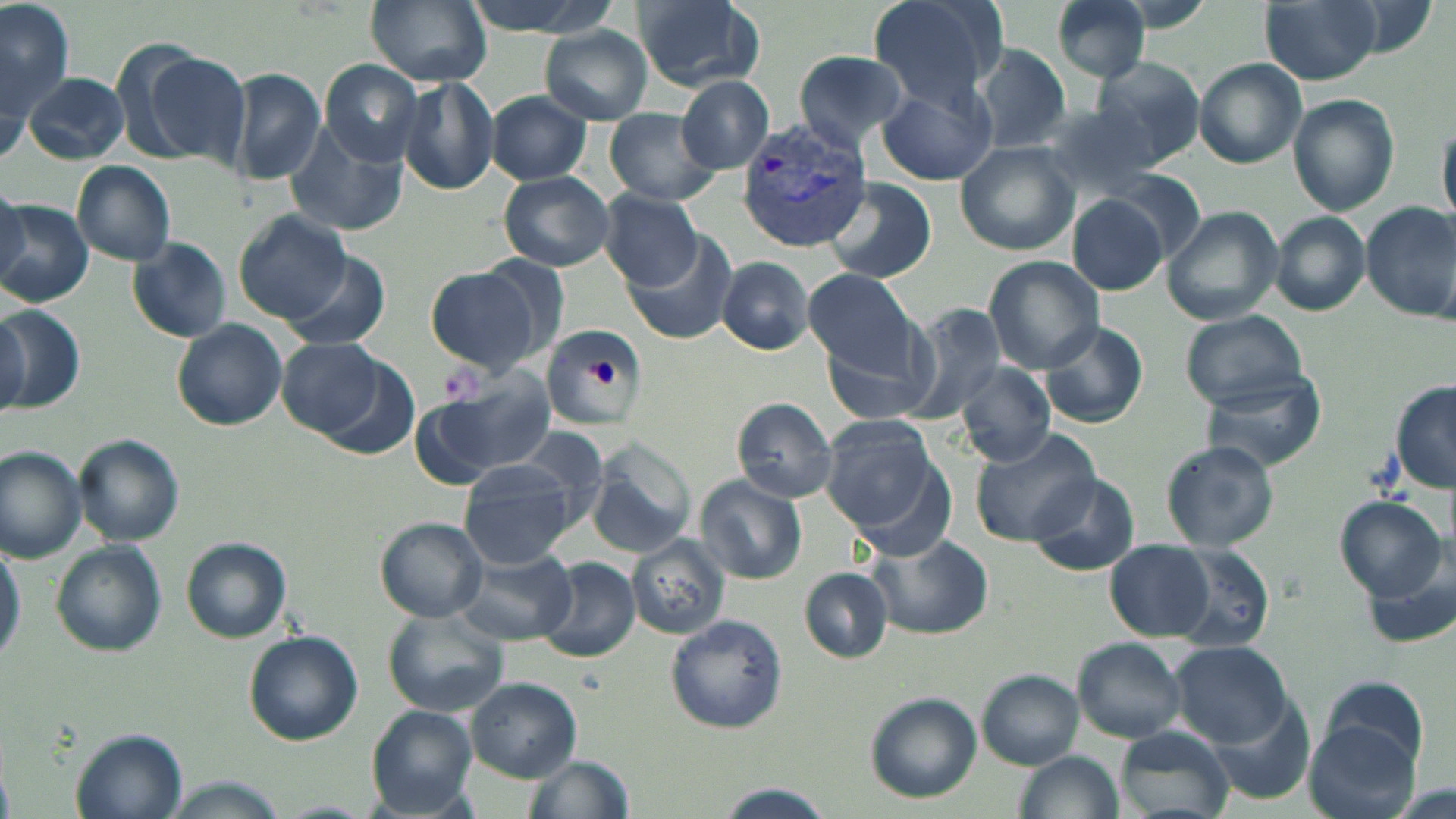
slide_level_diagnosis: Plasmodium vivax
field_of_view: single
magnification: 1000x
platelet_locations: 'approximate bounding boxes as (x1, y1, x2, y2) in pixels: (593, 356, 621, 388)'
uninfected_red_blood_cell_locations: 'approximate bounding boxes as (x1, y1, x2, y2) in pixels: (455, 0, 620, 38), (630, 0, 767, 94), (868, 0, 1008, 111), (1046, 0, 1155, 81), (1258, 0, 1383, 85), (1, 1, 76, 118), (364, 2, 490, 87), (539, 26, 654, 124), (976, 44, 1071, 152), (132, 47, 253, 166), (793, 49, 912, 153), (1088, 55, 1208, 168), (320, 59, 426, 163), (1194, 59, 1307, 167), (232, 69, 325, 185), (23, 71, 130, 165), (678, 76, 774, 173), (397, 77, 501, 196), (879, 77, 998, 185), (488, 91, 591, 185), (1287, 94, 1400, 215), (1030, 103, 1167, 204), (603, 109, 721, 205), (1437, 120, 1455, 231), (285, 121, 409, 236), (954, 142, 1079, 256), (73, 161, 176, 266), (498, 171, 615, 270), (827, 177, 940, 283), (0, 186, 29, 288), (600, 190, 704, 289), (1067, 197, 1169, 295), (0, 198, 94, 306), (1361, 201, 1456, 324), (1163, 204, 1285, 326), (234, 210, 351, 324), (1271, 212, 1371, 315), (623, 231, 737, 344), (127, 238, 230, 342), (285, 252, 391, 351), (717, 257, 815, 355), (983, 257, 1105, 371), (426, 266, 546, 374), (803, 266, 923, 378), (904, 304, 1008, 424), (0, 306, 82, 413), (1179, 309, 1308, 412), (0, 310, 30, 414), (818, 319, 946, 426), (1037, 319, 1150, 428), (172, 320, 287, 431), (538, 323, 653, 430), (278, 337, 389, 439), (956, 362, 1056, 467), (1201, 371, 1326, 472), (418, 378, 554, 483), (1391, 380, 1456, 491), (732, 398, 839, 502), (823, 417, 939, 531), (970, 427, 1102, 546), (74, 434, 185, 545), (1160, 440, 1280, 551), (587, 441, 696, 555), (0, 446, 88, 561), (455, 461, 578, 568), (1027, 471, 1141, 575), (697, 475, 807, 584), (1332, 494, 1446, 599), (376, 516, 487, 620), (626, 535, 729, 638), (867, 535, 990, 638), (0, 536, 23, 667), (181, 540, 291, 643), (51, 541, 166, 656), (1104, 542, 1212, 641), (1162, 544, 1275, 654), (454, 549, 578, 644), (1363, 552, 1456, 652), (539, 557, 641, 664), (800, 567, 893, 662), (382, 609, 508, 717), (664, 614, 787, 733), (243, 630, 363, 743), (1069, 635, 1188, 744), (1171, 640, 1292, 745), (975, 669, 1084, 768), (1319, 675, 1431, 774), (466, 677, 581, 782), (864, 693, 981, 803), (1207, 696, 1312, 801), (366, 706, 479, 815), (1304, 723, 1421, 819), (1114, 726, 1233, 819), (72, 728, 187, 818), (1016, 751, 1121, 819), (520, 754, 636, 819), (165, 777, 289, 819), (708, 783, 838, 819), (266, 801, 377, 818)'
image_size: 1456×819 pixels
preparation: thin blood smear
plasmodium_vivax_infected_red_blood_cell_locations: 'approximate bounding boxes as (x1, y1, x2, y2) in pixels: (736, 115, 875, 251)'
stain: May-Grünwald-Giemsa
modality: light microscopy